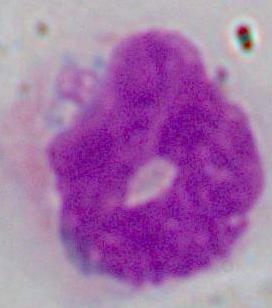

Summary:
  - Identification: white blood cell
  - Magnification: 1000x
  - Modality: micrograph